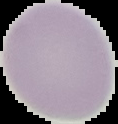

image size = 118×124 pixels
preparation = thin blood smear
malaria status = uninfected
image type = segmented cell region with the area outside set to black